Name the parasite shown.
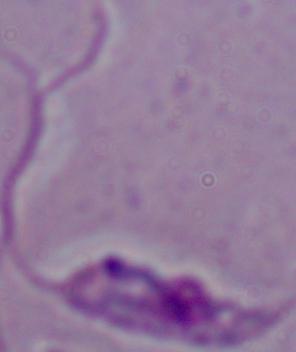
This is Leishmania.

Micrograph. 1000x magnification.